Locate every Plasmodium parasite.
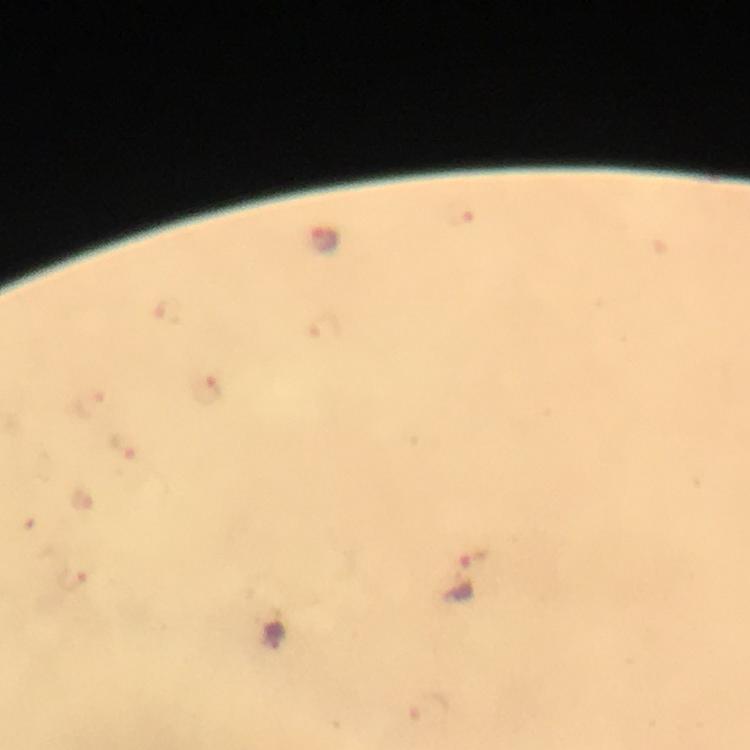

Approximate centers as [x, y] in pixels.
Plasmodium parasites: [326, 242], [171, 313], [326, 329], [208, 390], [90, 402], [125, 445], [463, 579], [75, 580].

Giemsa-stained preparation. From a malaria diagnostic workup. 100x magnification. Photographed through the microscope with a smartphone camera. Thick smear. Image is 750×750 pixels. Immersion oil applied. A crop from one field of view.